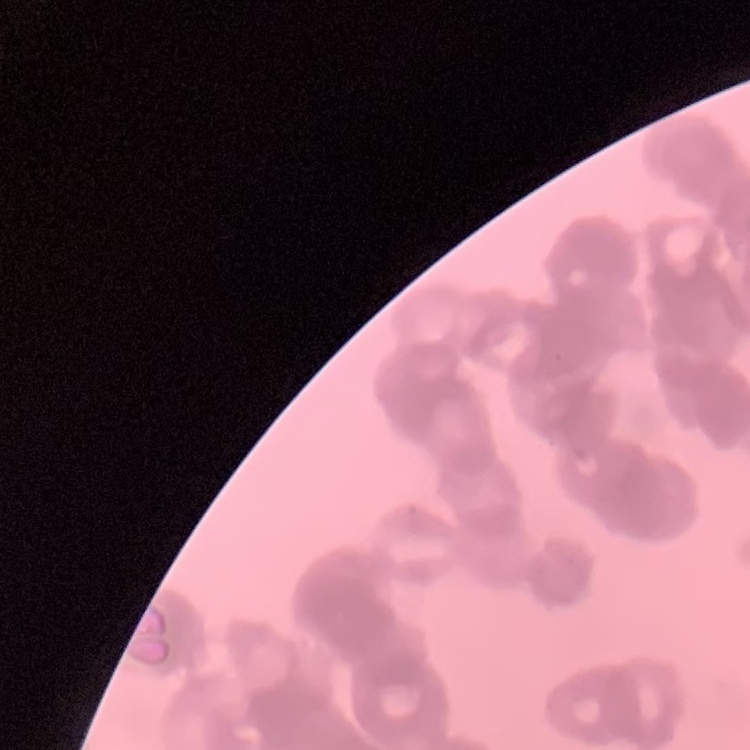
Summary:
  - Red blood cell morphology: rouleaux formation
  - Stain: Field's or Giemsa
  - Image type: square crop of a larger photomicrograph
  - Preparation: thin blood film